Assess the morphology of the erythrocytes.
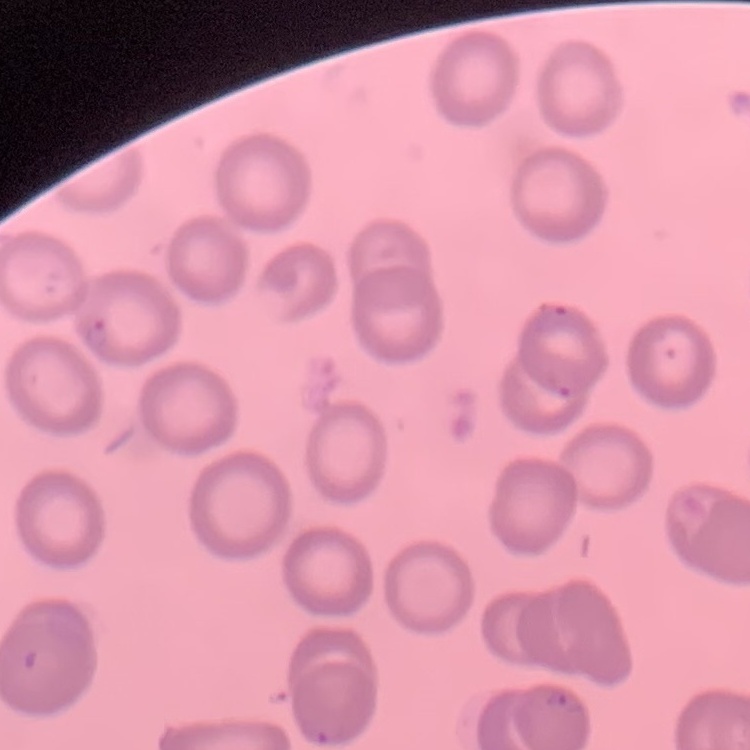

No rouleaux formation.

Square crop of a larger photomicrograph. Stained with either Field's or Giemsa. Thin blood film.